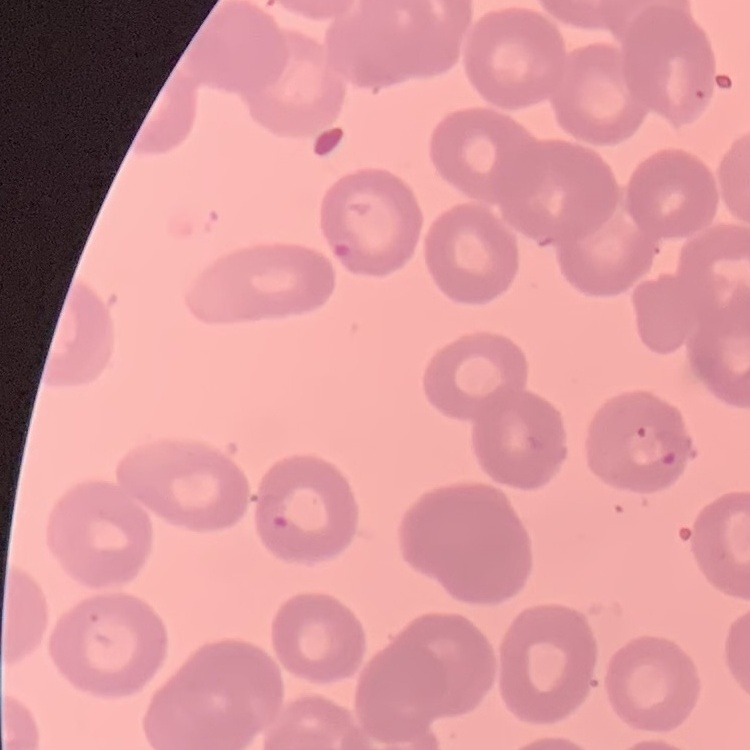

red blood cell morphology = no rouleaux formation
preparation = thin peripheral smear
image type = one tile cut from a larger photomicrograph
stain = Field's or Giemsa